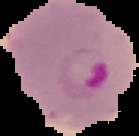
image type = segmented cell region on a black background
malaria status = parasitized
preparation = thin blood smear
image size = 139×136 pixels